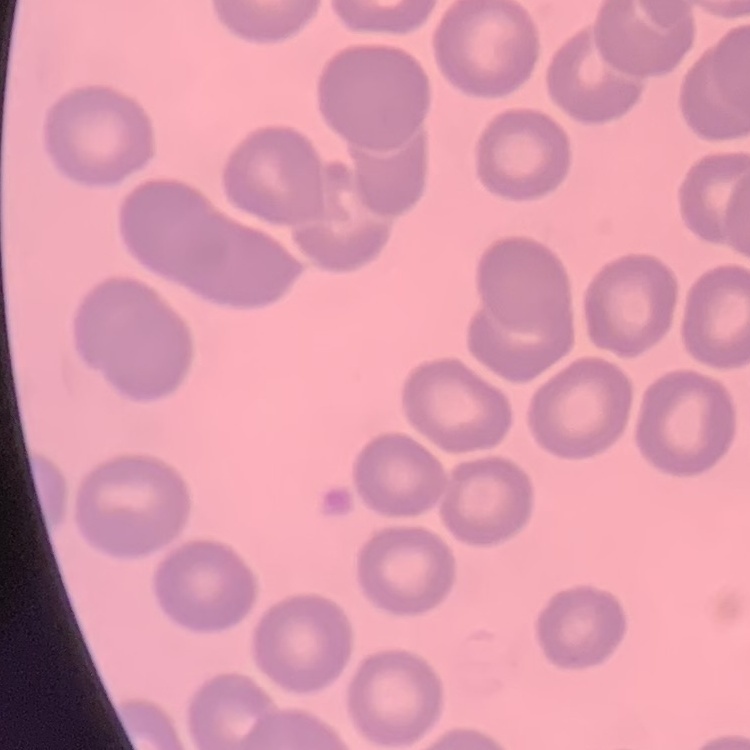

red blood cell morphology = no rouleaux formation
stain = Field's or Giemsa
image type = one tile cut from a larger photomicrograph
preparation = thin peripheral smear